State the preparation type.
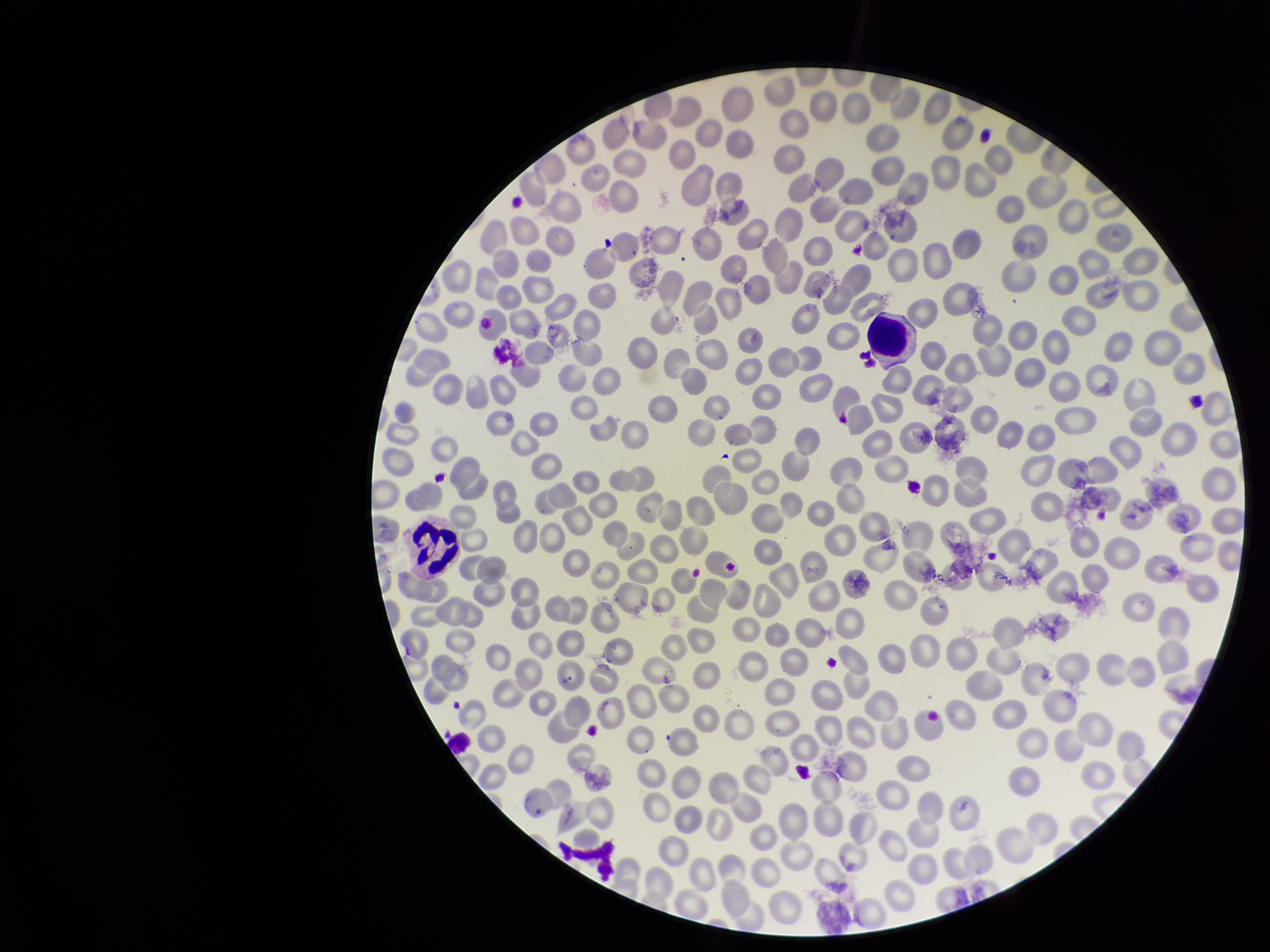

Thin.

Image is 1270×952 pixels. Parasitized red blood cells: none seen. Parasitized red blood cell count: 0. Patient malaria status: negative. Photographed through the microscope eyepiece with a smartphone camera. Red blood cell count: 293. One field from this slide. Stained with Giemsa.